Assess the morphology of the erythrocytes.
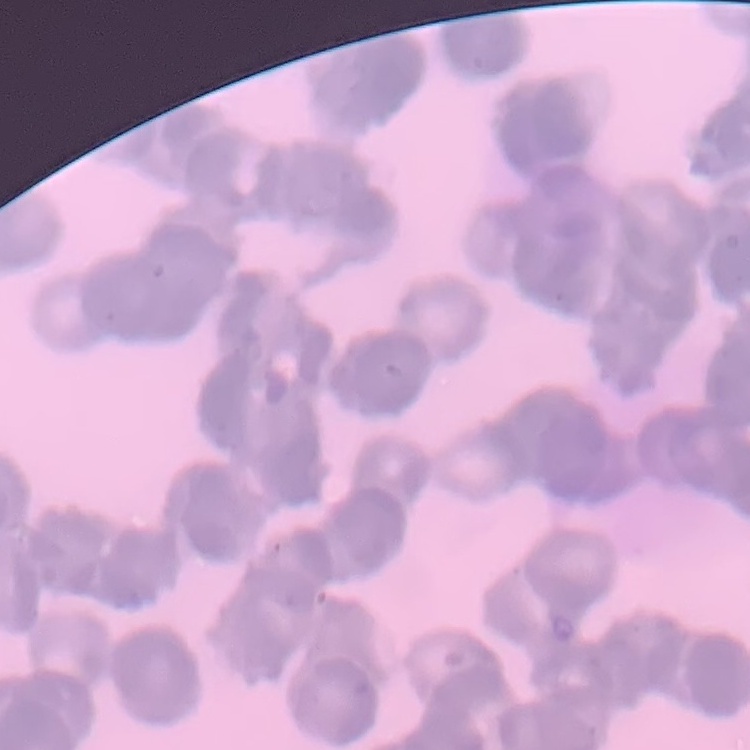
They show rouleaux formation.

Summary:
  - Preparation: thin blood film
  - Stain: Field's or Giemsa
  - Image type: one tile cut from a larger photomicrograph